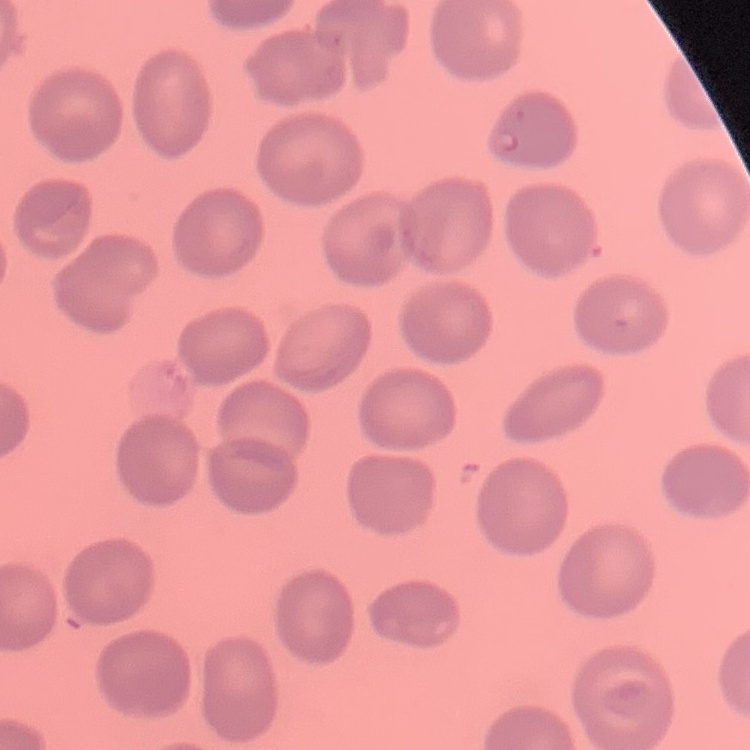

The erythrocytes show no rouleaux formation. Thin blood film. One tile cut from a larger photomicrograph. Field's or Giemsa stain.